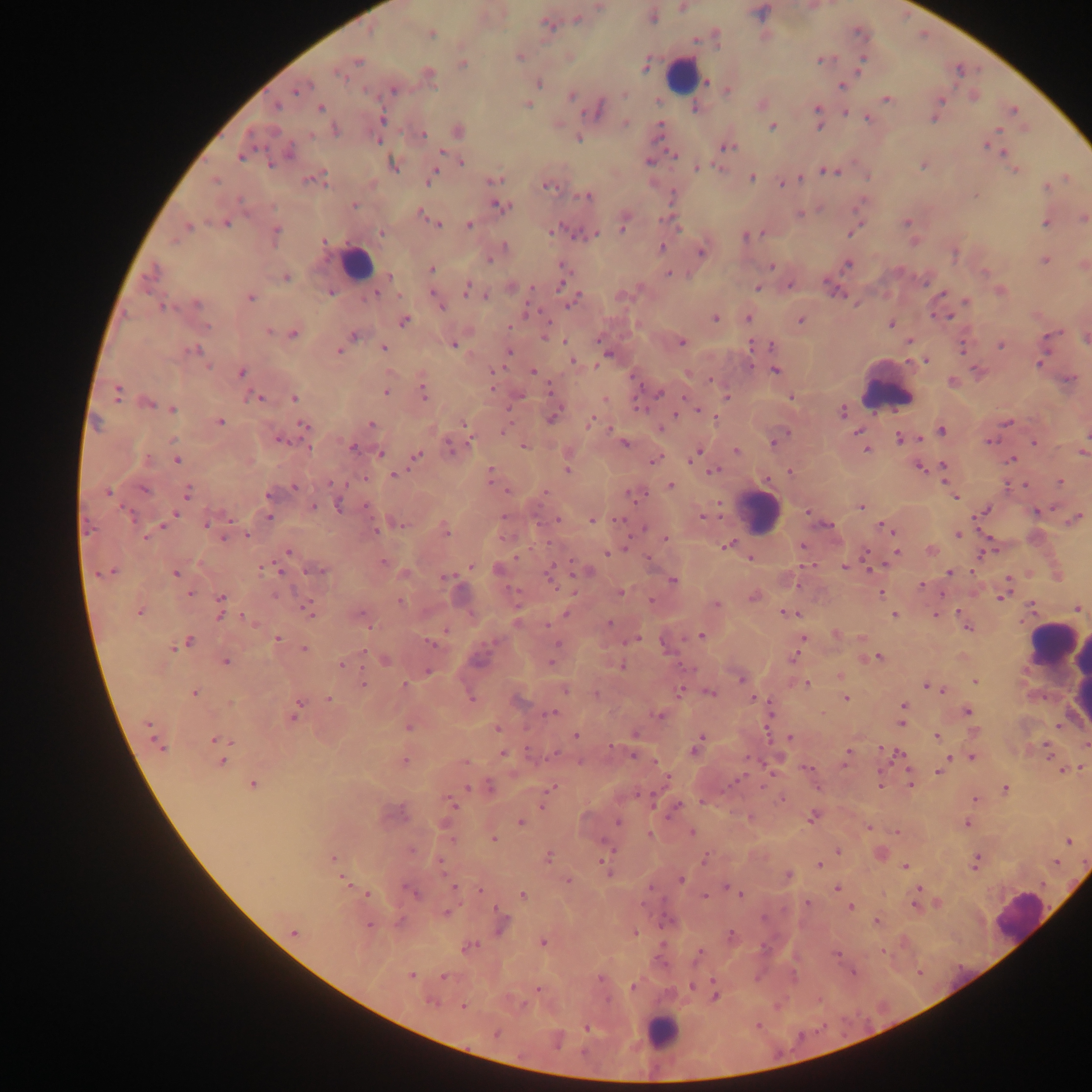 Approximate centers as {x, y} in pixels. Leukocyte locations: {680, 74}, {356, 264}, {887, 386}, {758, 512}, {1055, 644}, {1082, 674}, {1021, 917}, {661, 1032}. Malaria parasite locations: {599, 6}, {682, 7}, {652, 17}, {577, 19}, {547, 23}, {431, 33}, {520, 56}, {862, 59}, {357, 60}, {821, 60}, {462, 62}, {646, 66}, {858, 70}, {341, 72}, {427, 74}, {706, 81}, {538, 82}, {841, 86}, {298, 88}, {393, 89}, {727, 89}, {624, 93}, {571, 95}, {886, 99}, {938, 100}, {528, 104}, {761, 104}, {274, 105}, {320, 108}, {695, 108}, {597, 110}, {818, 110}, {1013, 111}, {844, 112}, {817, 116}, {934, 117}, {867, 118}, {382, 119}, {626, 122}, {820, 124}, {773, 126}, {659, 127}, {336, 130}, {997, 130}, {457, 131}, {310, 134}, {422, 135}, {578, 137}, {378, 140}, {985, 145}, {727, 146}, {1005, 152}, {674, 154}, {241, 155}, {461, 161}, {649, 161}, {392, 163}, {924, 164}, {1011, 167}, {697, 168}, {826, 170}, {1016, 170}, {433, 174}, {316, 178}, {751, 178}, {801, 178}, {495, 179}, {215, 180}, {782, 182}, {547, 185}, {1046, 186}, {588, 196}, {353, 205}, {498, 205}, {419, 213}, {799, 214}, {426, 217}, {1082, 218}, {624, 221}, {226, 222}, {907, 222}, {437, 223}, {1046, 223}, {469, 224}, {186, 227}, {552, 230}, {275, 232}, {381, 232}, {851, 232}, {583, 234}, {594, 234}, {745, 236}, {323, 241}, {503, 248}, {662, 248}, {701, 251}, {491, 256}, {1045, 260}, {847, 264}, {1083, 264}, {564, 265}, {771, 266}, {430, 269}, {669, 273}, {390, 276}, {285, 277}, {562, 282}, {790, 285}, {511, 286}, {467, 288}, {758, 288}, {999, 290}, {376, 292}, {941, 293}, {485, 295}, {249, 297}, {436, 298}, {573, 300}, {966, 302}, {196, 304}, {439, 304}, {162, 306}, {949, 316}, {715, 317}, {747, 317}, {801, 319}, {403, 320}, {890, 324}, {268, 331}, {293, 332}, {1051, 333}, {353, 335}, {1085, 338}, {909, 340}, {564, 342}, {453, 343}, {682, 343}, {751, 345}, {772, 345}, {1000, 345}, {383, 347}, {963, 347}, {342, 348}, {195, 350}, {338, 351}, {508, 352}, {609, 354}, {927, 359}, {572, 361}, {1040, 362}, {776, 370}, {533, 371}, {241, 372}, {1070, 378}, {710, 379}, {952, 381}, {492, 386}, {385, 391}, {424, 391}, {550, 391}, {116, 392}, {657, 392}, {791, 397}, {259, 398}, {294, 398}, {605, 398}, {727, 398}, {146, 403}, {172, 409}, {697, 410}, {841, 412}, {676, 413}, {554, 415}, {715, 416}, {590, 421}, {220, 422}, {1007, 422}, {370, 424}, {303, 426}, {465, 426}, {611, 428}, {660, 428}, {502, 430}, {941, 430}, {857, 432}, {898, 437}, {919, 438}, {279, 439}, {988, 441}, {625, 442}, {774, 442}, {1033, 442}, {523, 445}, {352, 447}, {451, 447}, {866, 450}, {736, 451}, {1081, 452}, {380, 453}, {695, 454}, {416, 456}, {176, 458}, {1011, 458}, {654, 459}, {567, 466}, {918, 466}, {943, 466}, {713, 470}, {789, 471}, {395, 474}, {490, 475}, {1060, 482}, {1024, 484}, {670, 485}, {294, 487}, {506, 490}, {108, 491}, {186, 492}, {951, 492}, {270, 493}, {634, 493}, {954, 497}, {339, 504}, {860, 506}, {313, 507}, {984, 511}, {1037, 511}, {808, 512}, {172, 516}, {701, 516}, {268, 517}, {1075, 518}, {557, 520}, {591, 520}, {209, 521}, {395, 522}, {164, 524}, {828, 525}, {884, 526}, {444, 529}, {958, 534}, {224, 535}, {247, 535}, {665, 538}, {727, 545}, {802, 546}, {864, 550}, {930, 550}, {287, 551}, {897, 551}, {983, 552}, {608, 553}, {750, 557}, {647, 559}, {382, 563}, {470, 566}, {844, 567}, {869, 568}, {316, 570}, {500, 570}, {587, 571}, {972, 571}, {106, 572}, {176, 573}, {948, 573}, {405, 574}, {551, 574}, {444, 578}, {1007, 579}, {671, 580}, {921, 584}, {189, 592}, {621, 592}, {881, 593}, {752, 596}, {1001, 597}, {401, 601}, {716, 604}, {1032, 606}, {220, 607}, {307, 608}, {1076, 608}, {139, 610}, {959, 612}, {567, 613}, {786, 613}, {894, 614}, {359, 615}, {936, 615}, {609, 623}, {968, 627}, {835, 633}, {701, 636}, {862, 637}, {802, 638}, {276, 639}, {633, 639}, {185, 642}, {432, 643}, {304, 648}, {798, 648}, {793, 657}, {879, 657}, {384, 658}, {225, 661}, {551, 662}, {341, 664}, {621, 665}, {426, 671}, {841, 675}, {741, 678}, {975, 682}, {363, 683}, {806, 684}, {927, 685}, {404, 686}, {565, 689}, {941, 689}, {681, 690}, {709, 692}, {194, 693}, {471, 697}, {754, 698}, {845, 698}, {329, 699}, {517, 700}, {903, 705}, {966, 711}, {294, 712}, {552, 712}, {660, 714}, {901, 722}, {408, 725}, {148, 726}, {498, 728}, {635, 734}, {576, 735}, {937, 736}, {790, 738}, {217, 740}, {1086, 744}, {698, 745}, {159, 746}, {610, 746}, {880, 748}, {1047, 751}, {502, 754}, {633, 754}, {847, 754}, {899, 754}, {949, 757}, {971, 757}, {221, 760}, {404, 761}, {464, 762}, {1082, 768}, {806, 769}, {1062, 769}, {939, 771}, {666, 779}, {252, 783}, {911, 783}, {879, 786}, {490, 788}, {551, 788}, {1004, 789}, {782, 798}, {974, 800}, {451, 801}, {544, 804}, {675, 807}, {391, 813}, {750, 817}, {812, 818}, {520, 822}, {618, 822}, {967, 824}, {867, 827}, {690, 832}, {897, 832}, {650, 834}, {492, 838}, {1068, 841}, {837, 851}, {880, 854}, {547, 857}, {332, 858}, {704, 859}, {1055, 861}, {439, 862}, {605, 863}, {975, 863}, {818, 865}, {905, 866}, {788, 875}, {681, 879}, {345, 880}, {568, 881}, {454, 887}, {727, 887}, {836, 888}, {918, 889}, {480, 890}, {413, 892}, {367, 893}, {522, 894}, {740, 894}, {704, 897}, {916, 897}, {807, 903}, {938, 904}, {915, 905}, {850, 907}, {445, 912}, {876, 921}, {500, 924}, {369, 925}, {293, 931}, {635, 932}, {731, 936}, {541, 942}, {468, 946}, {882, 951}, {698, 954}, {836, 954}, {853, 971}, {411, 975}, {444, 976}, {600, 977}, {714, 982}, {634, 986}, {693, 986}, {538, 989}, {708, 990}, {714, 995}, {431, 1001}, {463, 1006}, {587, 1027}, {496, 1032}. Thick blood film. Photographed through a microscope with a mobile-phone camera. Image is 1092×1092 pixels. Sample from Ghana. Single field of view.